Mark where leukocytes are.
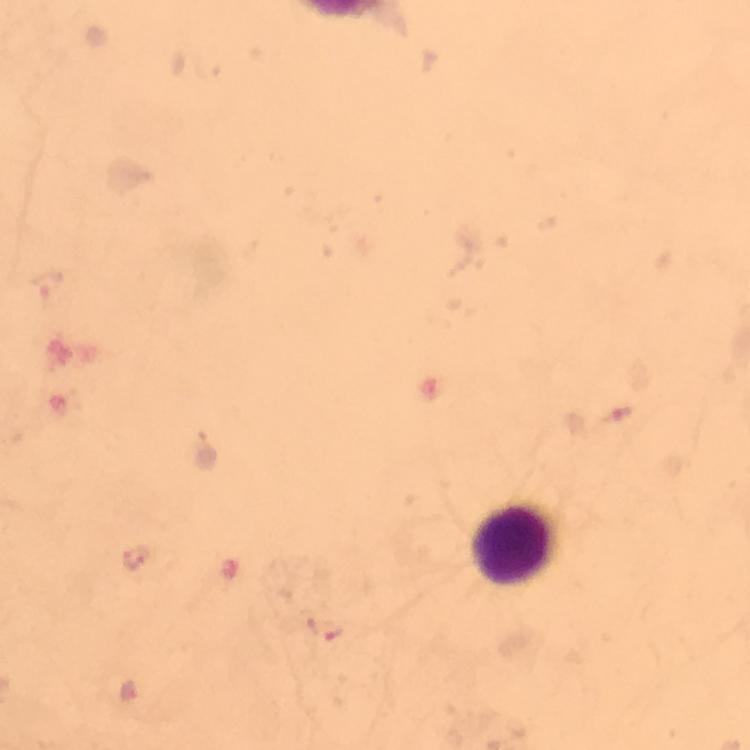

Approximate centers as [x, y] in pixels.
Leukocytes: [512, 541].

Plasmodium parasite locations: [135, 559]. 100x magnification. Giemsa-stained preparation. Image is 750×750 pixels. Cropped region of a single field of view. From a diagnostic examination for malaria. Immersion oil applied. Thick smear. Smartphone photograph taken through a microscope.